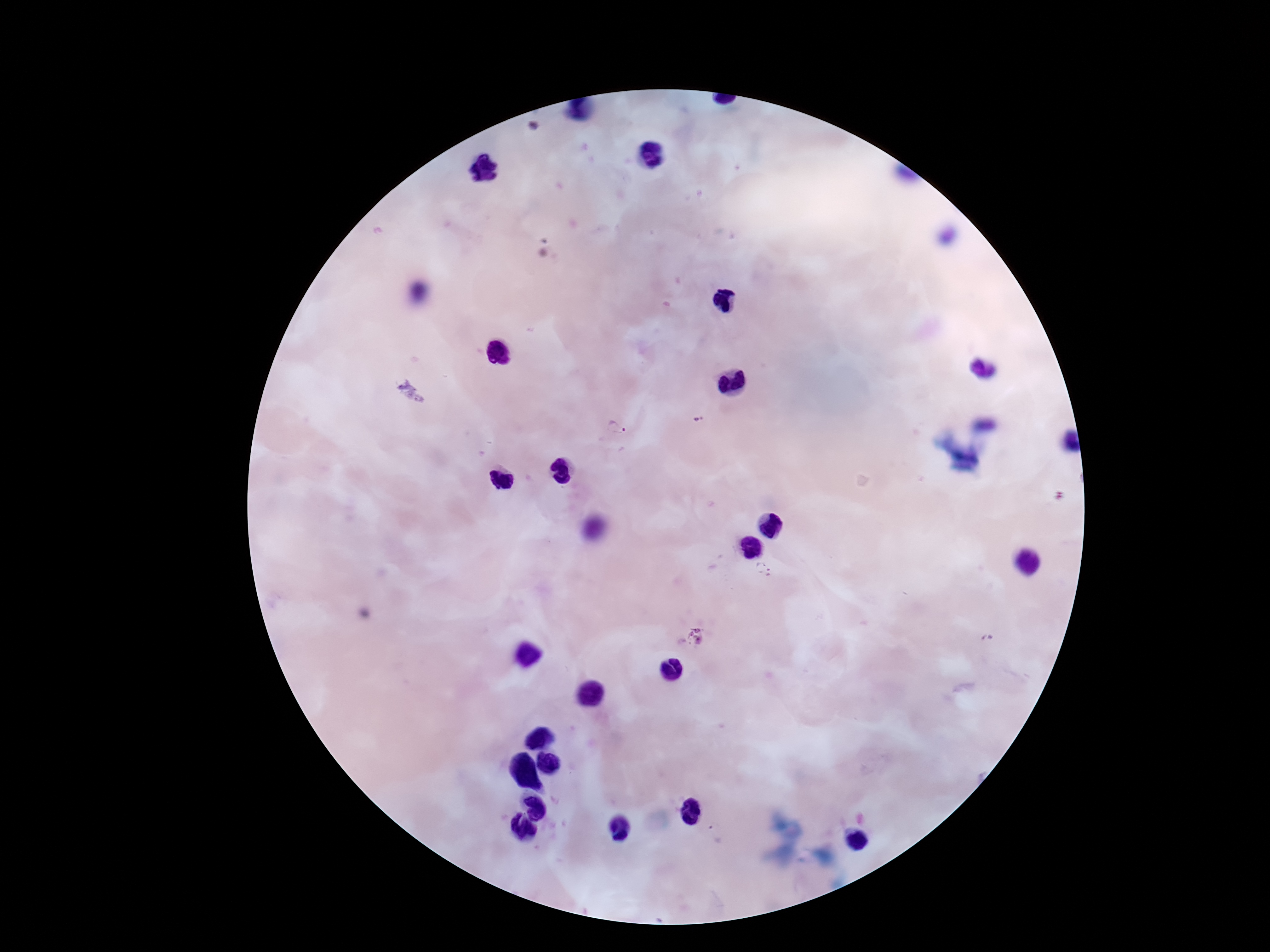
Approximate centers as (x, y) in pixels. Plasmodium parasite locations: (534, 126), (411, 393), (701, 419), (617, 427), (762, 569), (696, 636), (985, 639). Image is 1270×952 pixels. Photographed through the microscope eyepiece with a smartphone camera. 100x magnification. Patient malaria status: positive. Giemsa stain. Thick blood smear. Single field of view.